Locate and identify every blood parasite.
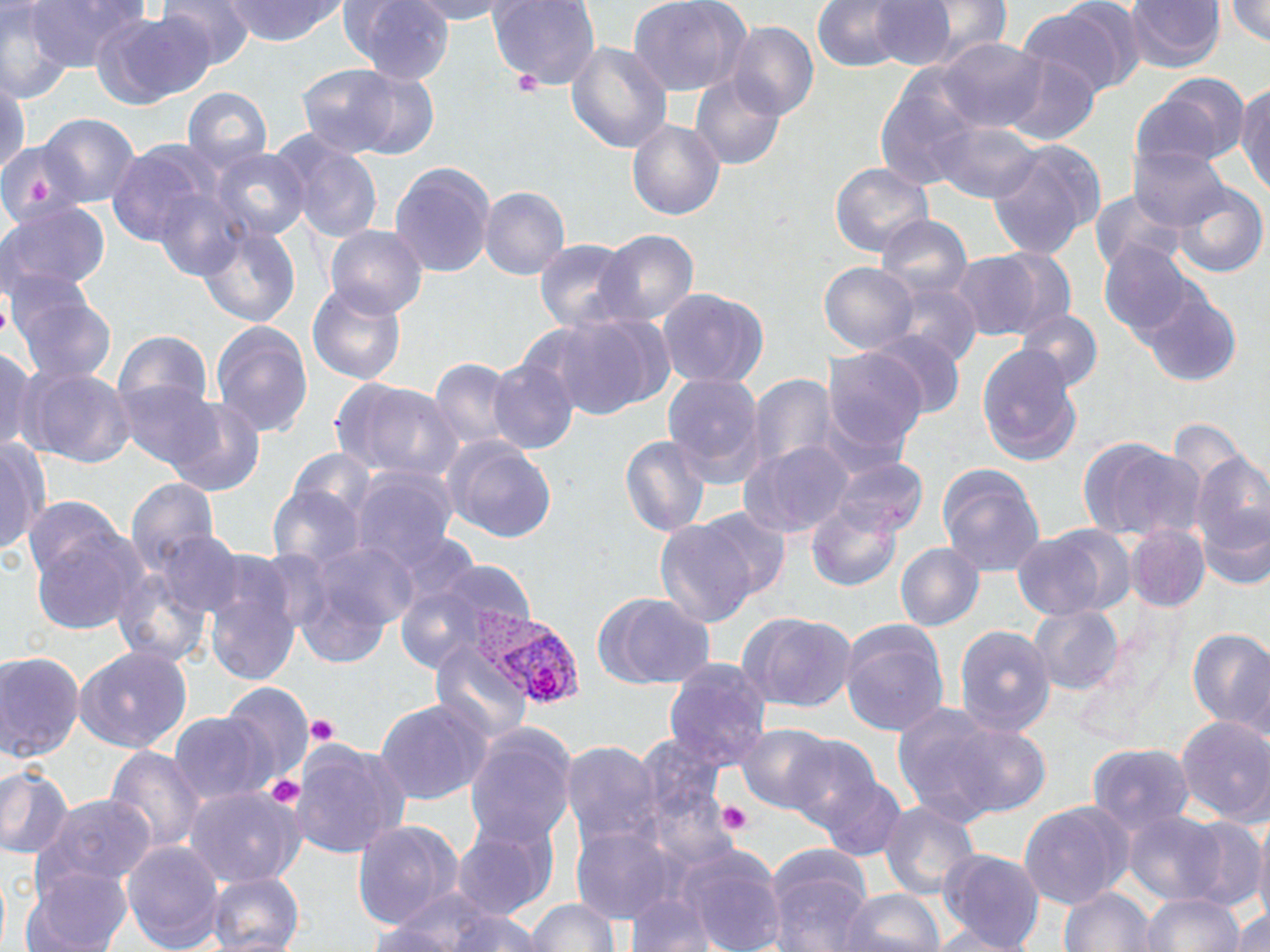
Approximate bounding boxes as (x1,y1)-(x2,y2) corner pairs in pixels.
Plasmodium vivax-infected red blood cells: (478,611)-(587,711).
No Plasmodium falciparum, Plasmodium ovale, Plasmodium malariae, Babesia divergens, or Trypanosoma brucei observed.

Uninfected red blood cell locations: (26,0)-(147,73), (156,0)-(257,70), (224,0)-(342,46), (342,0)-(454,83), (408,0)-(522,24), (488,0)-(601,92), (629,0)-(751,99), (1123,0)-(1227,75), (1225,0)-(1270,48), (866,1)-(961,72), (811,2)-(912,73), (902,2)-(1014,65), (0,3)-(76,103), (1019,3)-(1139,102), (95,11)-(208,110), (726,21)-(818,121), (937,37)-(1049,132), (566,41)-(672,153), (1000,49)-(1100,146), (297,63)-(429,158), (874,68)-(983,188), (1138,73)-(1250,170), (691,74)-(786,170), (0,76)-(30,178), (1236,82)-(1270,195), (182,86)-(273,171), (36,113)-(141,208), (627,120)-(725,220), (931,120)-(1041,204), (270,129)-(385,243), (0,138)-(85,224), (106,139)-(217,243), (988,140)-(1104,259), (1128,146)-(1230,230), (210,148)-(311,242), (390,162)-(496,279), (830,163)-(934,258), (1170,183)-(1268,279), (480,187)-(570,281), (153,188)-(248,281), (1089,190)-(1188,276), (0,202)-(111,297), (876,214)-(974,300), (197,226)-(301,328), (324,226)-(428,318), (595,230)-(699,327), (534,240)-(634,331), (1097,241)-(1204,341), (955,249)-(1067,342), (819,262)-(917,353), (886,280)-(981,368), (306,282)-(407,384), (11,287)-(117,385), (657,288)-(766,388), (1142,289)-(1242,388), (1015,309)-(1103,390), (537,312)-(670,420), (209,319)-(314,436), (113,330)-(213,419), (869,330)-(966,420), (976,345)-(1082,466), (0,347)-(36,456), (821,347)-(929,454), (429,357)-(516,451), (487,358)-(579,456), (20,365)-(136,468), (662,373)-(767,485), (746,373)-(842,472), (332,378)-(463,481), (112,379)-(219,468), (162,395)-(267,497), (617,435)-(711,537), (444,437)-(557,542), (1079,437)-(1200,541), (0,439)-(48,556), (741,440)-(855,538), (283,449)-(378,524), (1190,450)-(1270,567), (828,455)-(927,538), (937,463)-(1046,576), (349,465)-(460,569), (127,477)-(220,569), (268,485)-(365,569), (21,495)-(129,587), (1199,496)-(1270,592), (805,500)-(902,592), (692,506)-(792,605), (654,517)-(761,627), (1125,523)-(1210,613), (27,524)-(146,635), (1012,525)-(1130,620), (385,529)-(484,615), (153,531)-(244,616), (300,537)-(419,646), (895,541)-(984,631), (414,559)-(538,656), (112,565)-(211,667), (203,571)-(301,685), (390,578)-(503,675), (599,593)-(715,688), (1029,605)-(1125,694), (740,611)-(857,712), (839,620)-(951,736), (953,623)-(1057,733), (1187,628)-(1270,732), (431,643)-(533,742), (74,646)-(195,754), (0,650)-(86,761), (663,658)-(773,770), (218,681)-(316,783), (375,698)-(494,805), (893,704)-(1002,821), (170,712)-(270,804), (1175,716)-(1270,823), (942,722)-(1052,817), (737,723)-(838,812), (462,726)-(577,845), (784,733)-(882,830), (634,735)-(727,822), (290,739)-(408,860), (560,739)-(665,844), (1086,743)-(1195,831), (102,745)-(206,854), (0,764)-(73,858), (979,772)-(1095,899), (812,774)-(907,860), (184,785)-(306,887), (41,794)-(157,888), (1018,800)-(1131,908), (879,801)-(980,898), (1121,809)-(1237,907), (1253,810)-(1270,930), (1176,814)-(1266,912), (452,817)-(557,921), (351,821)-(465,932), (569,824)-(682,927), (120,840)-(225,951), (680,844)-(788,952), (764,847)-(875,952), (938,848)-(1046,952), (22,865)-(128,952), (206,872)-(304,952), (1058,888)-(1156,951), (841,889)-(946,952), (1142,893)-(1245,952), (625,895)-(716,951), (527,898)-(621,951), (1231,907)-(1269,949), (439,910)-(545,952), (364,923)-(473,952), (920,927)-(1042,950). Platelet locations: (513,69)-(543,96), (307,715)-(338,747), (263,775)-(304,808), (717,801)-(753,835). Slide-level diagnosis: Plasmodium vivax. One field of a larger specimen. 1000x magnification. May-Grünwald-Giemsa-stained preparation. Thin blood smear. Optical microscopy. Image is 1270×952 pixels.